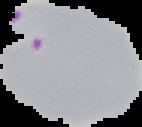
Summary:
  - Image size: 142×127 pixels
  - Result: Plasmodium parasites identified
  - Image type: segmented cell region on a black background
  - Preparation: thin blood film